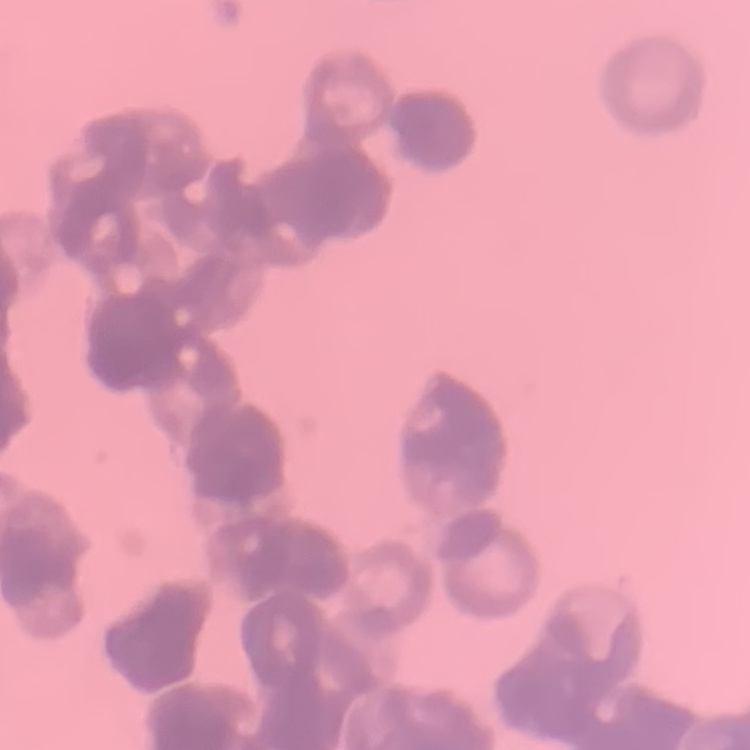

erythrocyte morphology = rouleaux formation
preparation = thin peripheral smear
stain = Field's or Giemsa
image type = one tile cut from a larger photomicrograph